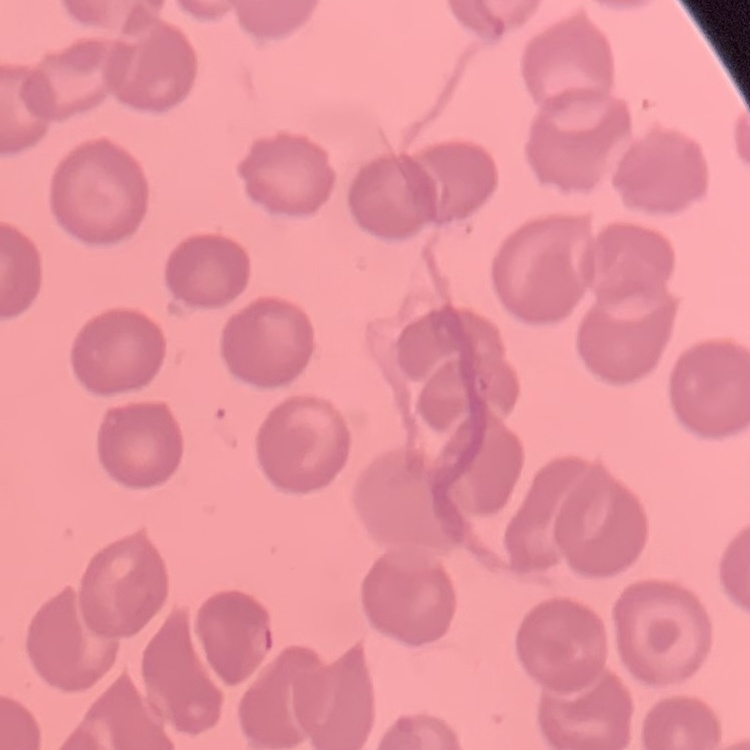
The erythrocytes show no rouleaux formation. Square crop of a larger photomicrograph. Stained with either Field's or Giemsa. Thin blood smear.